Assess this cell for malaria.
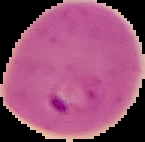

It is parasitized.

image_size: 145×142 pixels
image_type: segmented cell region with the area outside set to black
preparation: thin blood film